Assess this cell for malaria.
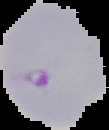

Parasitized.

From a thin blood film. Image is 109×130 pixels. The area outside the segmented cell region is set to black.